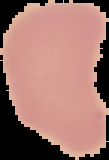
image type = cell region segmented out of the field of view; surrounding area masked to black
image size = 109×160 pixels
malaria status = uninfected
preparation = thin blood film